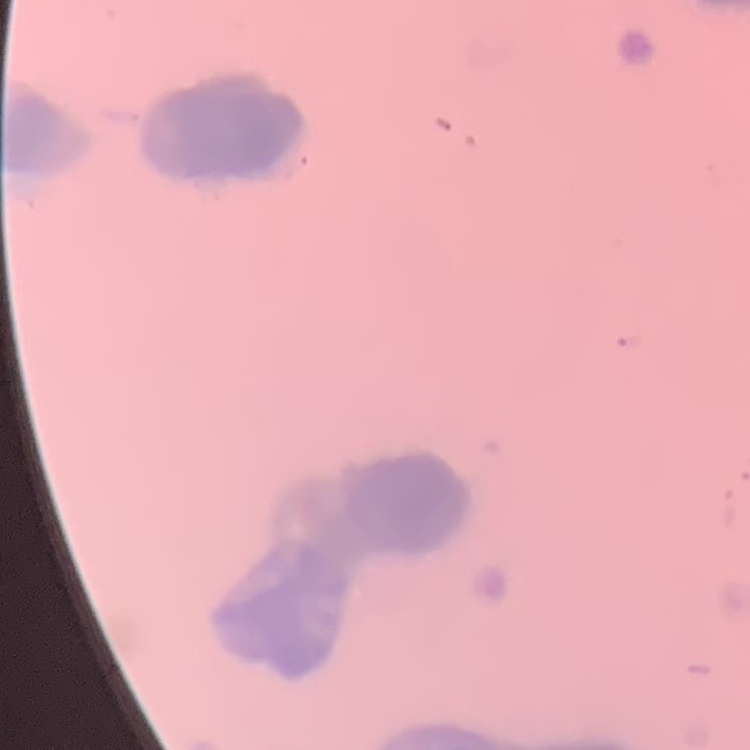

erythrocyte_morphology: rouleaux formation
stain: Field's or Giemsa
image_type: one tile cut from a larger photomicrograph
preparation: thin peripheral smear